Assess this cell for malaria.
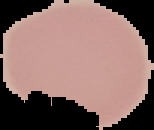

Uninfected.

Summary:
  - Image size: 154×130 pixels
  - Image type: cell region segmented out of the field of view; surrounding area masked to black
  - Preparation: thin blood smear